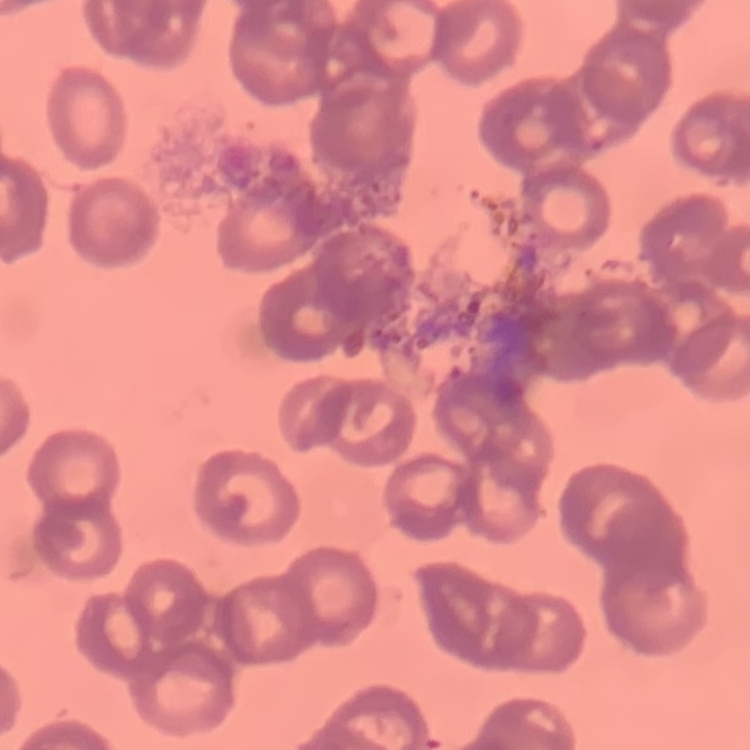
Summary:
  - Red blood cell morphology: rouleaux formation
  - Image type: one tile cut from a larger photomicrograph
  - Stain: Field's or Giemsa
  - Preparation: thin blood film